Identify the blood parasite species.
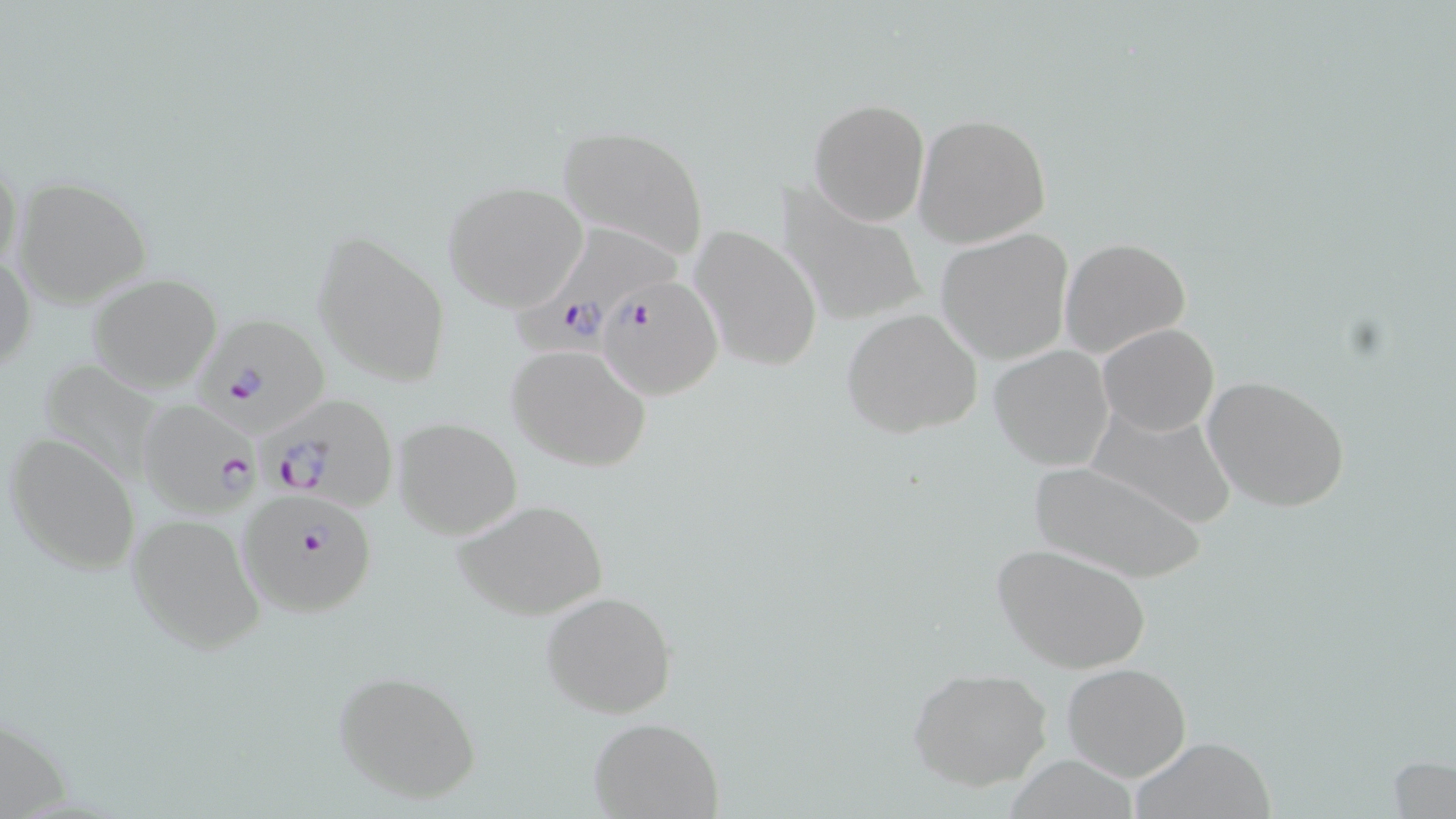

Plasmodium falciparum.

Summary:
  - Coordinate format: approximate bounding boxes as (x1,y1)-(x2,y2) corner pairs in pixels
  - Uninfected red blood cell locations: (807,98)-(929,226), (913,113)-(1052,249), (556,125)-(709,264), (0,154)-(25,284), (12,176)-(153,309), (441,180)-(590,312), (775,183)-(927,327), (687,225)-(824,374), (310,228)-(452,389), (937,230)-(1073,364), (1060,237)-(1190,358), (1,250)-(36,376), (87,274)-(224,392), (841,307)-(983,438), (1098,322)-(1220,436), (505,343)-(652,470), (990,345)-(1115,470), (35,357)-(165,483), (1201,374)-(1349,513), (1086,405)-(1240,530), (393,418)-(522,539), (5,431)-(142,575), (1027,461)-(1210,583), (453,497)-(609,623), (125,509)-(266,653), (992,542)-(1152,674), (541,590)-(676,718), (1062,662)-(1191,782), (333,668)-(483,805), (907,668)-(1054,791), (588,717)-(724,819), (1131,736)-(1278,818), (1388,753)-(1455,817)
  - Plasmodium falciparum-infected red blood cell locations: (508,229)-(685,355), (598,274)-(723,400), (196,315)-(332,433), (263,394)-(399,512), (136,399)-(258,517), (237,489)-(379,617)
  - Magnification: 1000x
  - Image size: 1456×819 pixels
  - Preparation: thin blood film
  - Field of view: one of a larger specimen
  - Stain: May-Grünwald-Giemsa
  - Modality: light microscopy